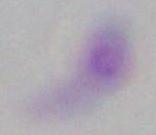
modality: micrograph
magnification: 1000x
identification: Toxoplasma gondii